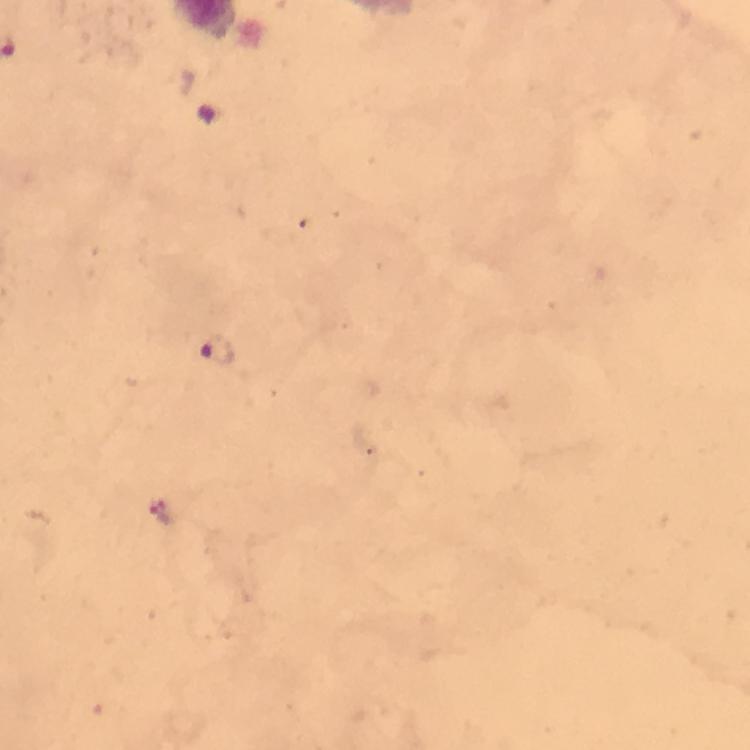
Approximate centers as (x, y) in pixels.
Summary:
  - Plasmodium parasite locations: (216, 351), (162, 513)
  - Preparation: thick smear
  - Capture: smartphone camera through the microscope
  - Stain: Giemsa
  - Context: from a malaria diagnostic workup
  - Image size: 750×750 pixels
  - Immersion oil: used
  - Cropped from: one field of view
  - Magnification: 100x